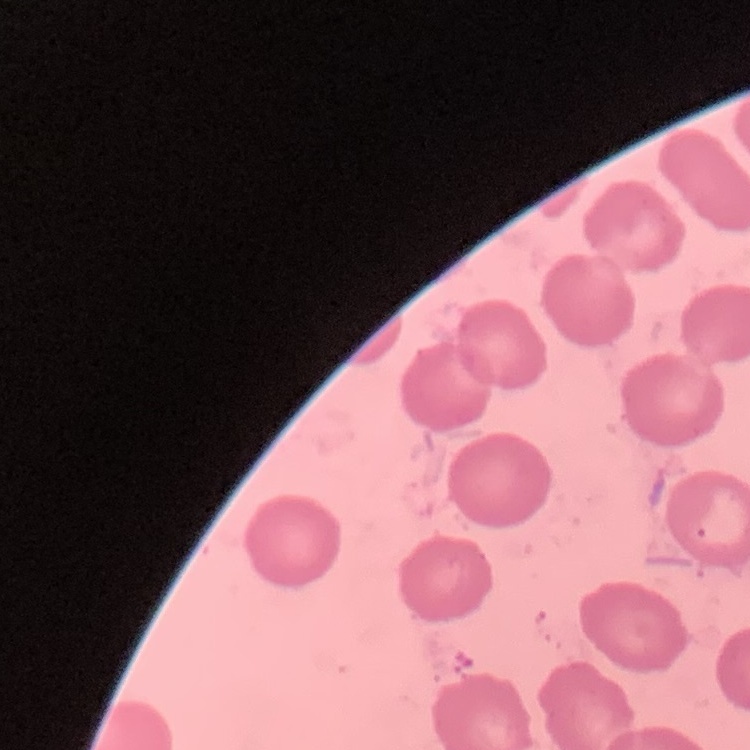
The erythrocytes exhibit no rouleaux formation. Stained with either Field's or Giemsa. Thin peripheral smear. One tile cut from a larger photomicrograph.